State which cell type is depicted.
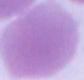

An erythrocyte.

magnification = 1000x
modality = micrograph